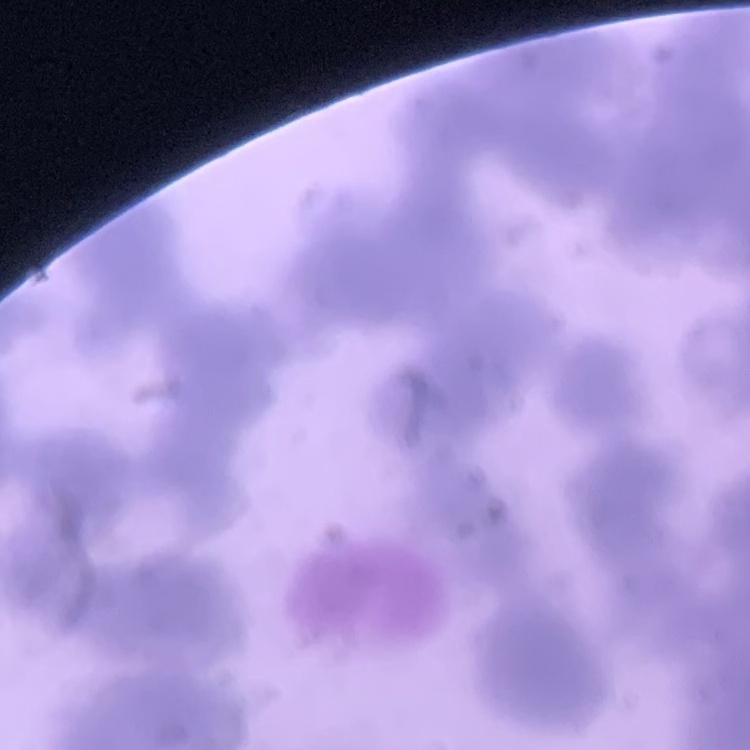
Summary:
  - Erythrocyte morphology: rouleaux formation
  - Preparation: thin blood film
  - Stain: Field's or Giemsa
  - Image type: one tile cut from a larger photomicrograph